Report the malaria status of this cell.
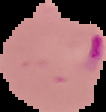
Parasitized.

Summary:
  - Preparation: thin blood film
  - Image type: segmented cell region on a black background
  - Image size: 106×112 pixels